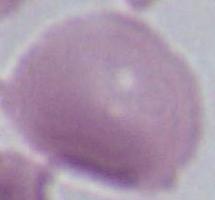

Captured at 1000x magnification. Photomicrograph. An erythrocyte is shown.